State which parasite is depicted.
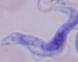

This is a trypanosome.

Summary:
  - Magnification: 1000x
  - Modality: photomicrograph